Report the malaria status of this cell.
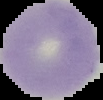
Uninfected.

image type = segmented cell region with the area outside set to black
preparation = thin blood smear
image size = 103×100 pixels